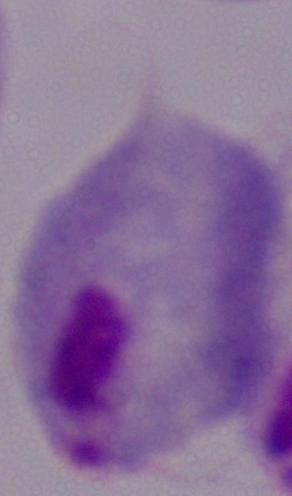

{
  "magnification": "1000x",
  "identification": "trichomonad",
  "modality": "photomicrograph"
}